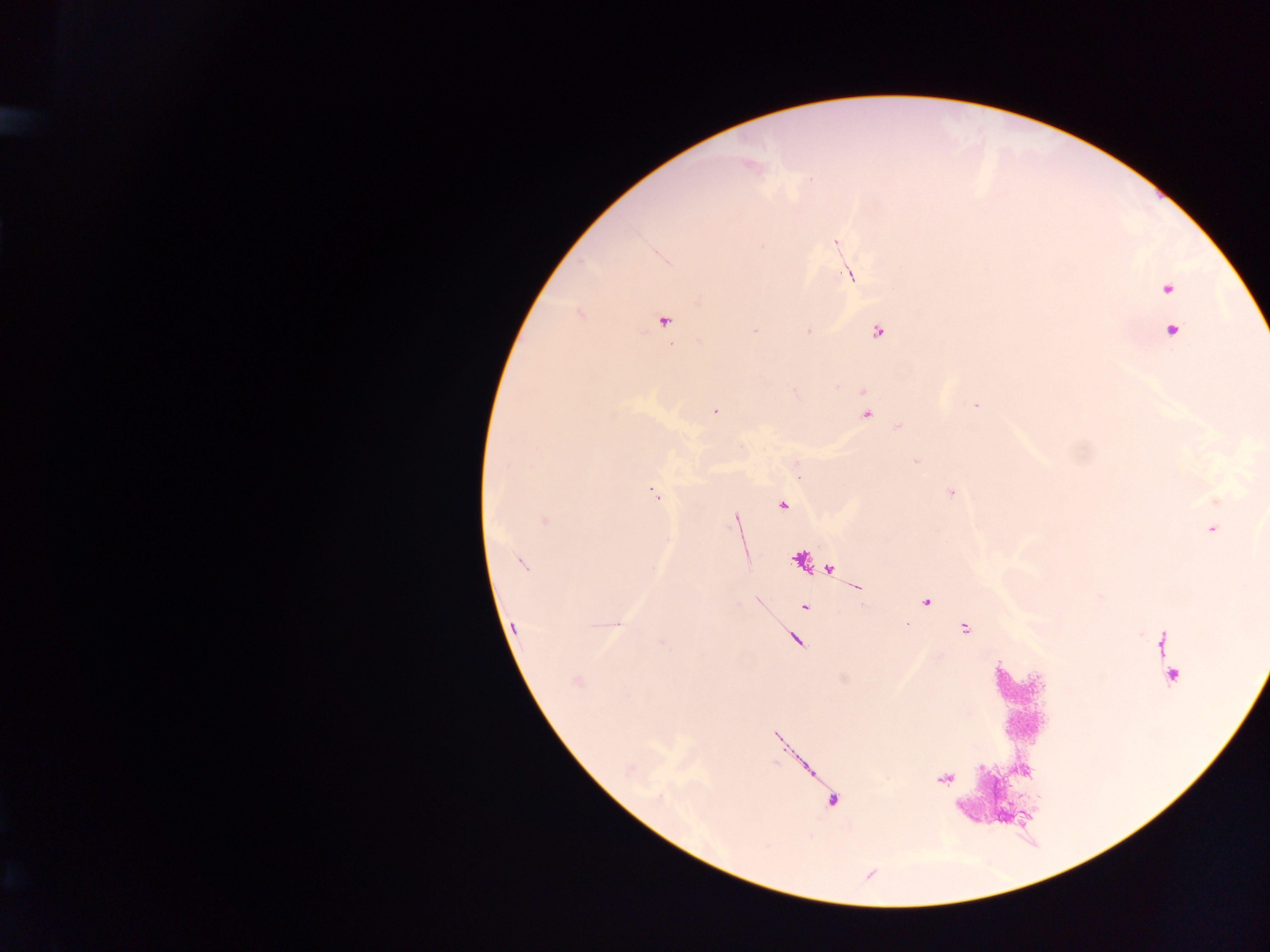

Approximate centers as (x, y) in pixels.
Summary:
  - Malaria parasite locations: (836, 242), (850, 275), (1167, 288), (663, 320), (1172, 330), (877, 332), (976, 405), (866, 415), (782, 505), (736, 520), (1211, 529), (926, 602), (805, 607), (616, 624), (514, 626)
  - Country: Ghana
  - Capture: mobile-phone photograph through a microscope
  - Field of view: single
  - Preparation: thick blood film
  - Image size: 1270×952 pixels